Point out each leukocyte.
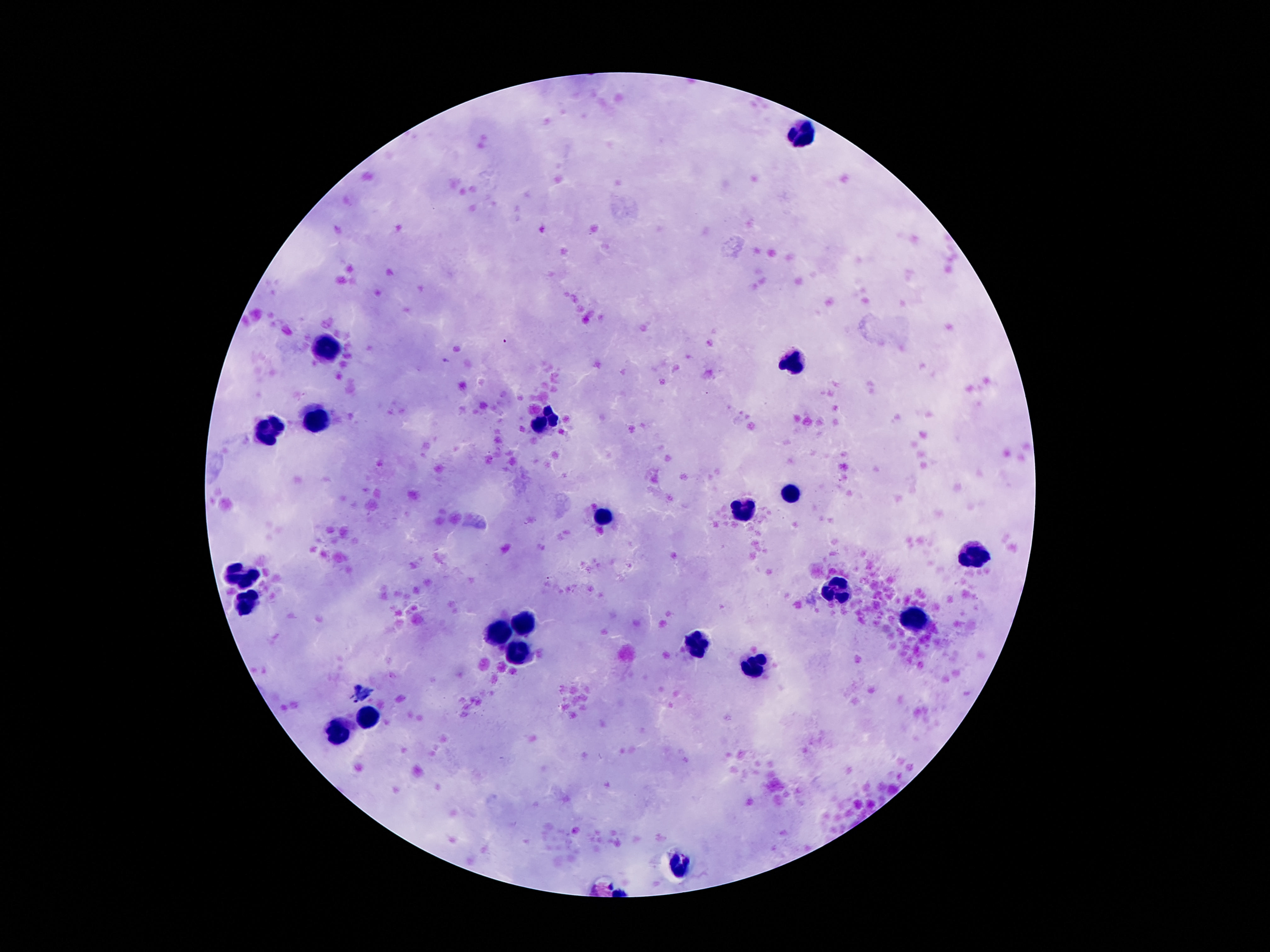

Approximate centers as [x, y] in pixels.
Leukocytes: [803, 129], [329, 344], [794, 358], [318, 416], [546, 421], [266, 430], [791, 491], [747, 509], [605, 518], [974, 551], [240, 572], [838, 593], [250, 598], [915, 619], [523, 626], [497, 635], [698, 645], [521, 647], [754, 668], [367, 714], [339, 733], [679, 868].

Summary:
  - Stain: Giemsa
  - Magnification: 100x
  - Field of view: single
  - Patient malaria status: uninfected
  - Preparation: thick peripheral-blood smear
  - Capture: smartphone camera through the microscope eyepiece
  - Image size: 1270×952 pixels